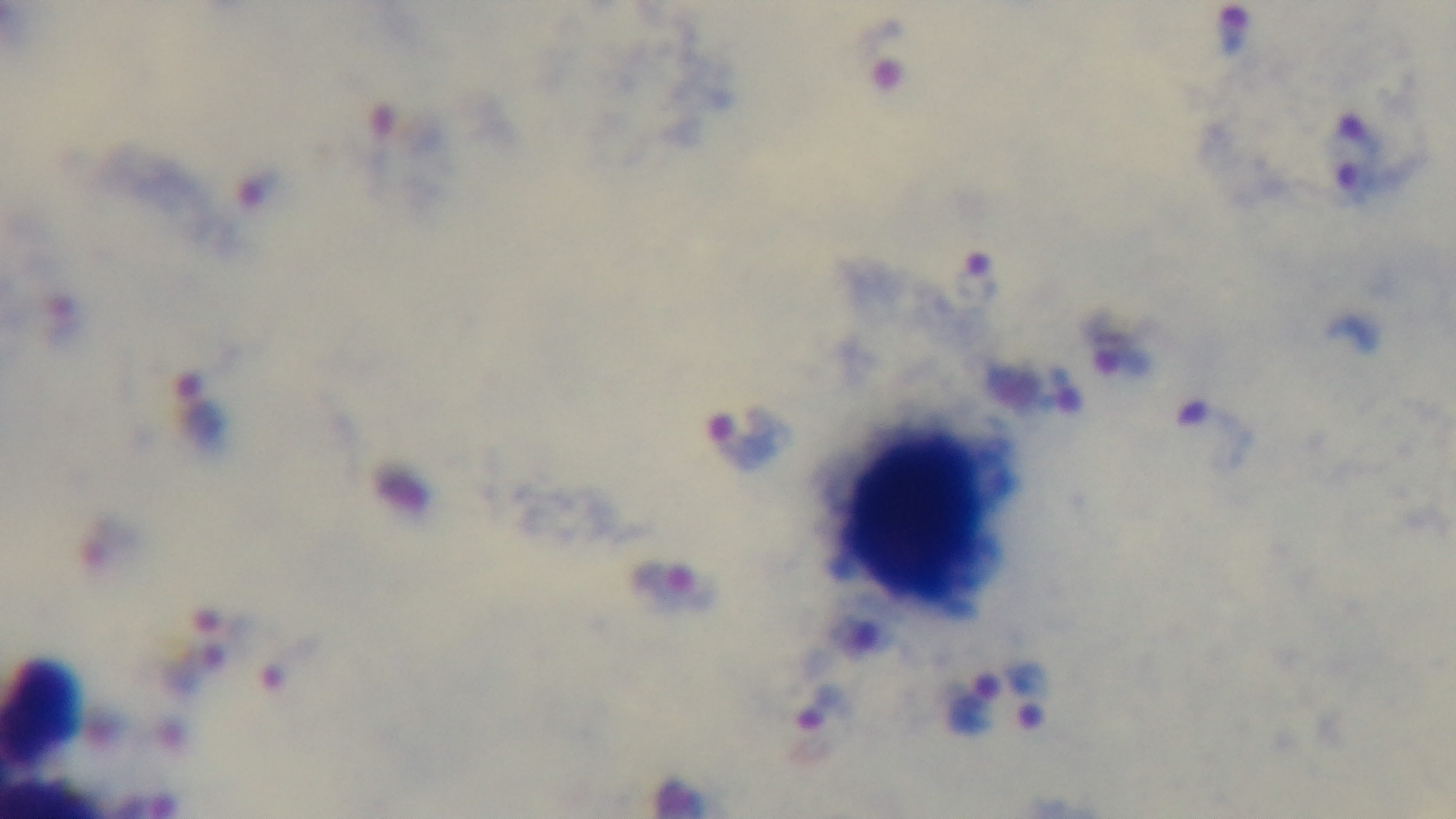

preparation = thick
stain = Giemsa
field of view = one from the slide
objective = 100x oil immersion
capture = mounted 4K digital camera
malaria status = infected
modality = light microscopy